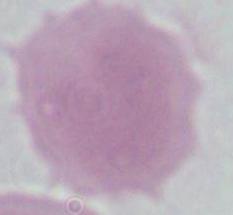

identification = red blood cell
modality = photomicrograph
magnification = 1000x